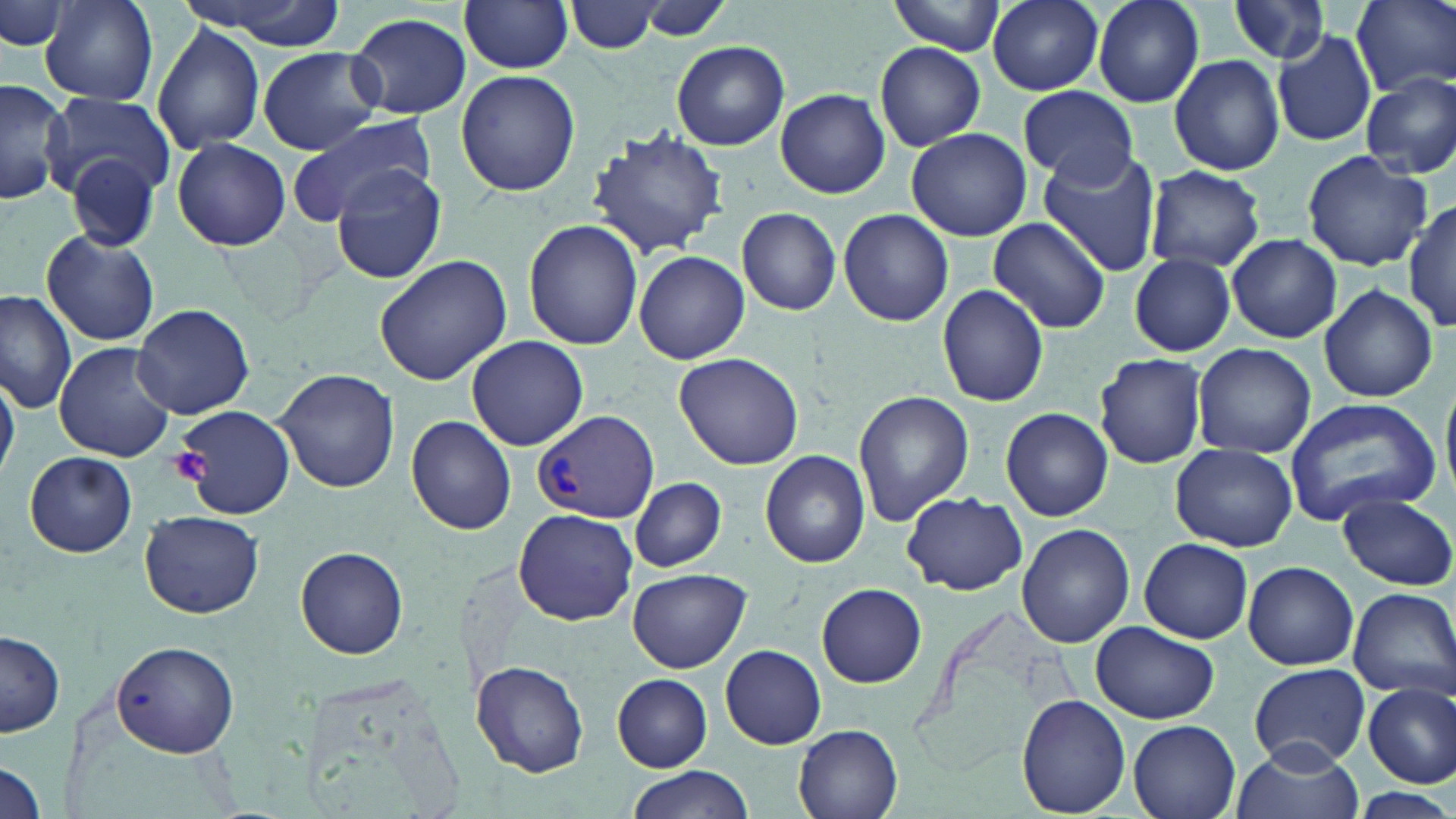

slide_level_diagnosis: Plasmodium vivax
stain: May-Grünwald-Giemsa
modality: optical microscopy
platelet_locations: 'approximate bounding boxes as named x1/y1/x2/y2 corners in pixels: (x1=169, y1=446, x2=212, y2=486)'
field_of_view: one of a larger specimen
magnification: 1000x
uninfected_red_blood_cell_locations: 'approximate bounding boxes as named x1/y1/x2/y2 corners in pixels: (x1=177, y1=0, x2=347, y2=48), (x1=459, y1=0, x2=574, y2=74), (x1=888, y1=0, x2=1008, y2=55), (x1=988, y1=0, x2=1104, y2=94), (x1=1092, y1=0, x2=1208, y2=109), (x1=1228, y1=0, x2=1335, y2=66), (x1=1354, y1=0, x2=1456, y2=99), (x1=42, y1=1, x2=158, y2=105), (x1=567, y1=1, x2=664, y2=53), (x1=623, y1=1, x2=740, y2=43), (x1=2, y1=2, x2=70, y2=53), (x1=347, y1=13, x2=471, y2=120), (x1=151, y1=22, x2=266, y2=155), (x1=1272, y1=28, x2=1377, y2=147), (x1=671, y1=40, x2=790, y2=151), (x1=875, y1=42, x2=987, y2=150), (x1=257, y1=46, x2=383, y2=154), (x1=1169, y1=54, x2=1284, y2=174), (x1=456, y1=69, x2=580, y2=196), (x1=1360, y1=73, x2=1456, y2=179), (x1=0, y1=79, x2=73, y2=208), (x1=1019, y1=86, x2=1137, y2=184), (x1=776, y1=88, x2=888, y2=199), (x1=46, y1=92, x2=175, y2=202), (x1=288, y1=112, x2=436, y2=225), (x1=906, y1=128, x2=1031, y2=240), (x1=590, y1=129, x2=732, y2=257), (x1=171, y1=138, x2=292, y2=251), (x1=1037, y1=147, x2=1164, y2=276), (x1=64, y1=151, x2=159, y2=253), (x1=1302, y1=151, x2=1432, y2=271), (x1=1144, y1=166, x2=1264, y2=273), (x1=333, y1=167, x2=447, y2=285), (x1=1405, y1=198, x2=1456, y2=334), (x1=737, y1=207, x2=841, y2=315), (x1=839, y1=208, x2=954, y2=326), (x1=988, y1=217, x2=1110, y2=334), (x1=524, y1=220, x2=644, y2=351), (x1=42, y1=229, x2=159, y2=347), (x1=1226, y1=234, x2=1342, y2=344), (x1=634, y1=250, x2=749, y2=364), (x1=373, y1=253, x2=513, y2=386), (x1=1129, y1=254, x2=1236, y2=356), (x1=1318, y1=283, x2=1439, y2=404), (x1=937, y1=284, x2=1049, y2=405), (x1=0, y1=289, x2=77, y2=414), (x1=134, y1=303, x2=257, y2=419), (x1=466, y1=336, x2=588, y2=451), (x1=54, y1=341, x2=178, y2=464), (x1=1191, y1=342, x2=1316, y2=460), (x1=673, y1=352, x2=805, y2=470), (x1=1096, y1=353, x2=1207, y2=467), (x1=272, y1=368, x2=399, y2=495), (x1=0, y1=371, x2=21, y2=479), (x1=853, y1=389, x2=974, y2=525), (x1=1283, y1=398, x2=1442, y2=521), (x1=170, y1=404, x2=297, y2=517), (x1=1001, y1=407, x2=1113, y2=522), (x1=408, y1=413, x2=518, y2=535), (x1=1170, y1=442, x2=1299, y2=551), (x1=760, y1=450, x2=870, y2=568), (x1=23, y1=451, x2=137, y2=558), (x1=629, y1=477, x2=727, y2=572), (x1=902, y1=492, x2=1026, y2=595), (x1=1337, y1=493, x2=1455, y2=590), (x1=512, y1=507, x2=639, y2=626), (x1=140, y1=509, x2=264, y2=618), (x1=1017, y1=524, x2=1136, y2=649), (x1=1138, y1=538, x2=1252, y2=643), (x1=296, y1=547, x2=409, y2=658), (x1=1243, y1=561, x2=1358, y2=671), (x1=626, y1=568, x2=749, y2=673), (x1=817, y1=583, x2=928, y2=688), (x1=1348, y1=586, x2=1456, y2=699), (x1=915, y1=598, x2=1083, y2=773), (x1=1091, y1=621, x2=1220, y2=724), (x1=1, y1=630, x2=65, y2=737), (x1=109, y1=642, x2=241, y2=757), (x1=719, y1=644, x2=826, y2=750), (x1=471, y1=659, x2=590, y2=777), (x1=1248, y1=664, x2=1372, y2=768), (x1=612, y1=674, x2=712, y2=771), (x1=1364, y1=681, x2=1455, y2=789), (x1=1016, y1=695, x2=1131, y2=816), (x1=1129, y1=720, x2=1243, y2=819), (x1=793, y1=722, x2=904, y2=819), (x1=1232, y1=741, x2=1364, y2=819), (x1=0, y1=761, x2=45, y2=816), (x1=624, y1=767, x2=753, y2=819), (x1=1350, y1=788, x2=1456, y2=818)'
plasmodium_vivax_infected_red_blood_cell_locations: 'approximate bounding boxes as named x1/y1/x2/y2 corners in pixels: (x1=533, y1=410, x2=659, y2=524)'
image_size: 1456×819 pixels
preparation: thin blood film